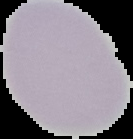
Summary:
  - Image type: cell region segmented out of the field of view; surrounding area masked to black
  - Preparation: thin blood film
  - Result: negative for malaria parasites
  - Image size: 133×139 pixels